Assess the morphology of the red blood cells.
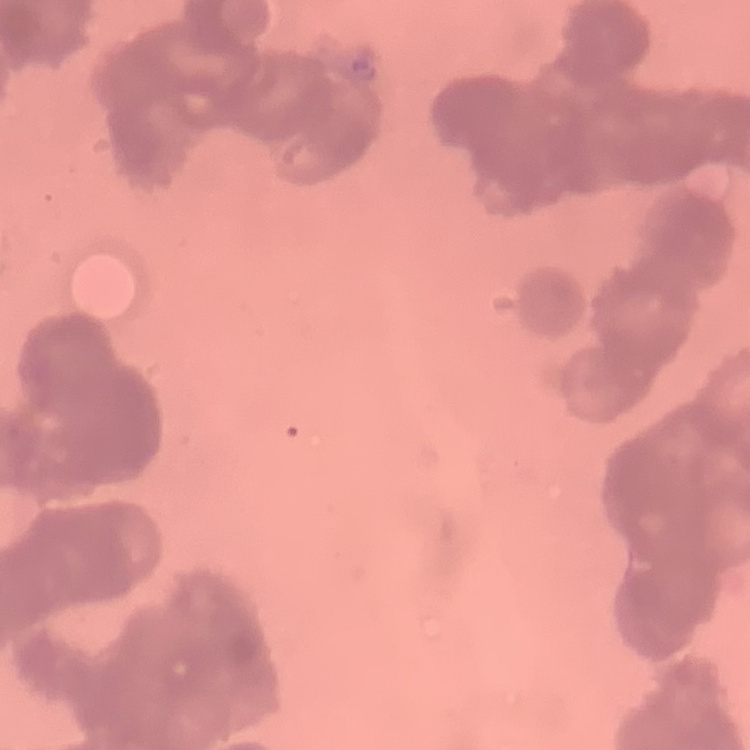
Rouleaux formation.

Summary:
  - Stain: Field's or Giemsa
  - Image type: square crop of a larger photomicrograph
  - Preparation: thin blood film